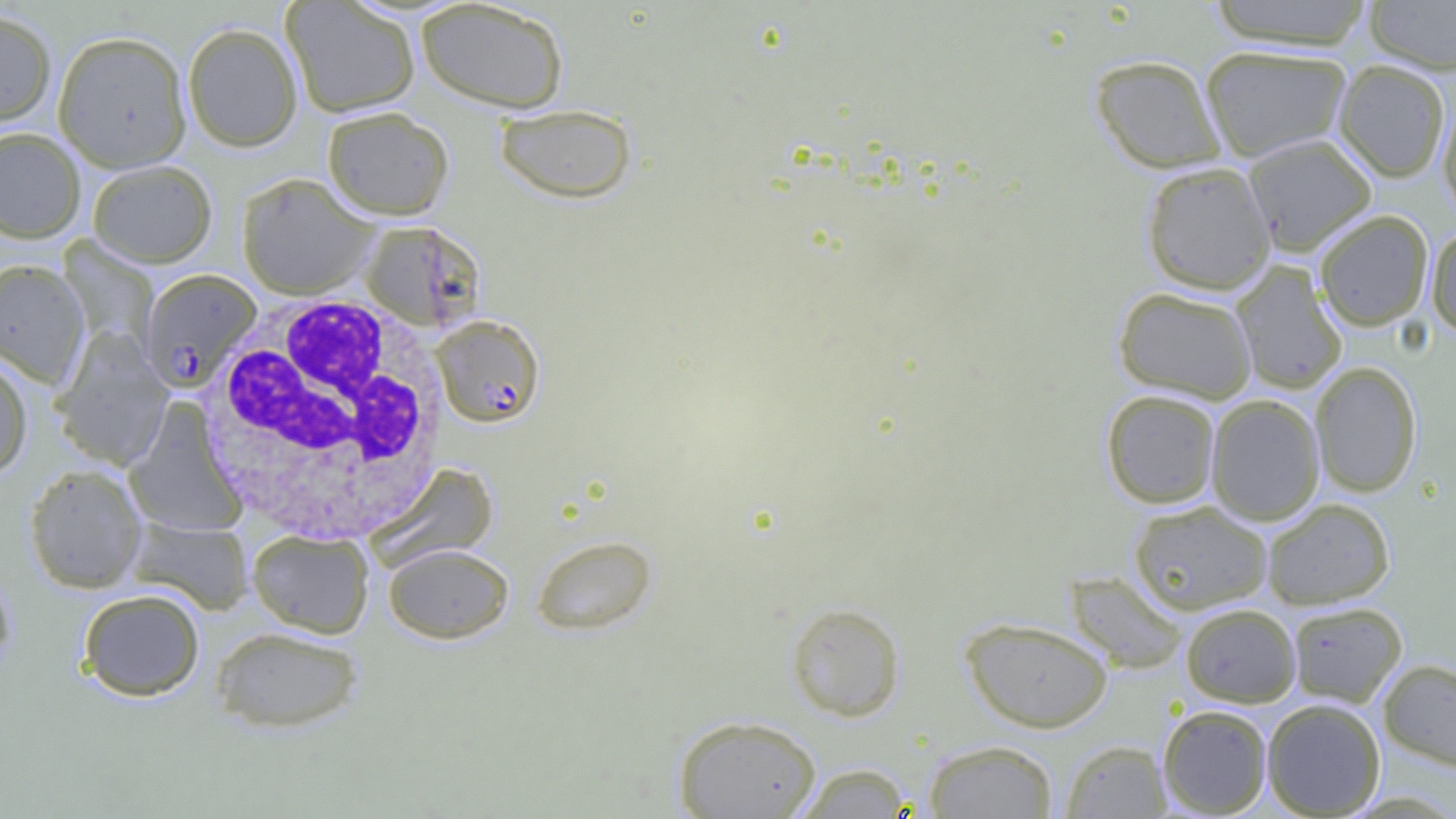
Approximate bounding boxes as [x1, y1, x2, y2] in pixels. Plasmodium falciparum-infected red blood cell locations: [139, 270, 261, 392], [431, 315, 545, 428]. Uninfected red blood cell locations: [280, 0, 421, 118], [415, 0, 570, 113], [1206, 0, 1376, 50], [1363, 1, 1456, 75], [0, 9, 57, 130], [182, 22, 303, 152], [52, 30, 193, 172], [1199, 45, 1353, 162], [1089, 54, 1227, 174], [1334, 60, 1451, 183], [1437, 93, 1456, 223], [494, 103, 637, 204], [321, 106, 454, 220], [0, 127, 86, 243], [1243, 133, 1377, 256], [87, 159, 218, 268], [1140, 161, 1276, 295], [237, 173, 378, 299], [1314, 209, 1434, 331], [360, 220, 487, 333], [1427, 225, 1456, 338], [0, 259, 90, 388], [1230, 261, 1347, 394], [1113, 286, 1258, 403], [52, 331, 173, 470], [0, 355, 34, 479], [1309, 361, 1422, 498], [1100, 389, 1221, 508], [1206, 394, 1325, 526], [124, 402, 247, 538], [364, 462, 499, 572], [24, 464, 147, 593], [1262, 498, 1395, 610], [1128, 500, 1272, 614], [126, 517, 254, 614], [247, 529, 374, 638], [531, 534, 658, 635], [383, 543, 514, 644], [0, 561, 17, 679], [1065, 571, 1189, 674], [77, 589, 205, 701], [785, 601, 906, 721], [1287, 601, 1407, 706], [1181, 604, 1301, 707], [960, 616, 1114, 733], [209, 626, 364, 733], [1378, 658, 1456, 774], [1261, 698, 1386, 817], [1157, 704, 1273, 817], [672, 714, 823, 819], [922, 739, 1059, 818], [1060, 739, 1172, 818], [790, 762, 915, 818]. White blood cell locations: [198, 288, 451, 539], [121, 394, 266, 541]. Slide-level diagnosis: Plasmodium falciparum. Thin blood film. One field of a larger specimen. Captured at 1000x magnification. Optical microscopy. Image is 1456×819 pixels.